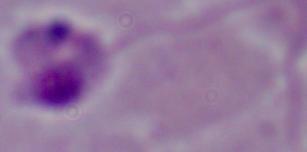

Micrograph. A Leishmania parasite is seen. Captured at 1000x magnification.